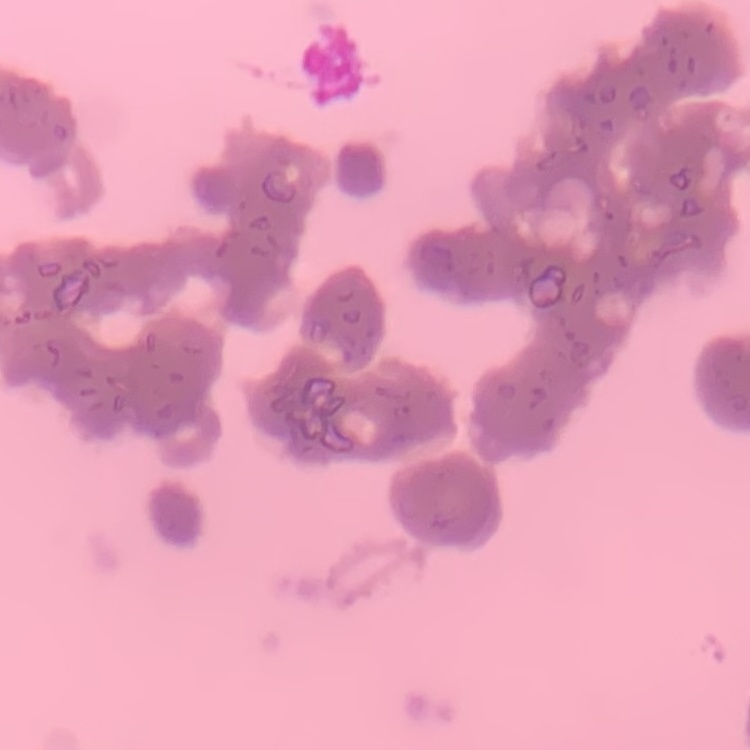
erythrocyte morphology = rouleaux formation
preparation = thin peripheral smear
stain = Field's or Giemsa
image type = one tile cut from a larger photomicrograph